Classify this cell by malaria status.
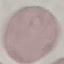

Uninfected.

Automatically extracted cell patch, resized to 64 × 64 pixels. Thin blood smear. Acquired by smartphone through the microscope eyepiece. Giemsa stain.